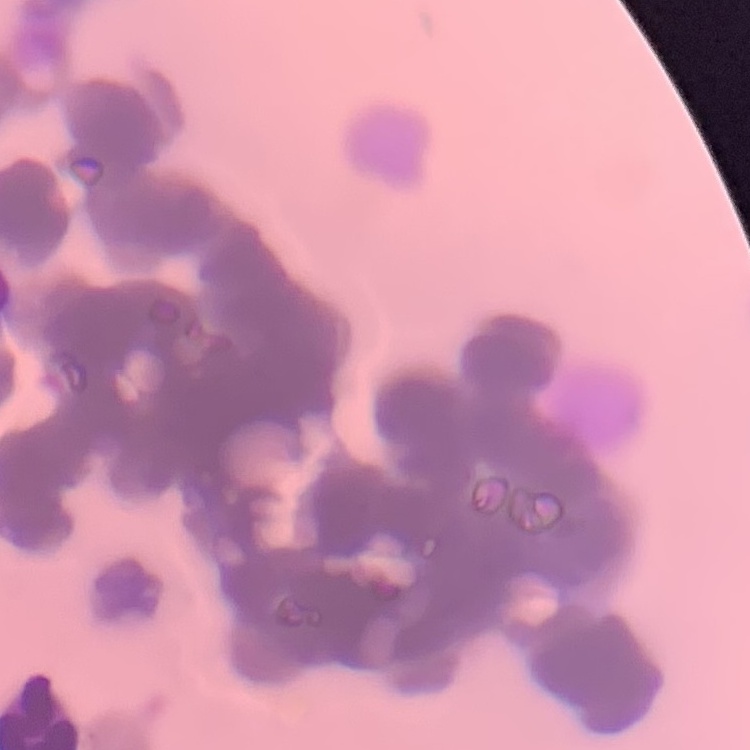
The erythrocytes exhibit rouleaux formation. Stained with either Field's or Giemsa. Thin blood smear. Square crop of a larger photomicrograph.